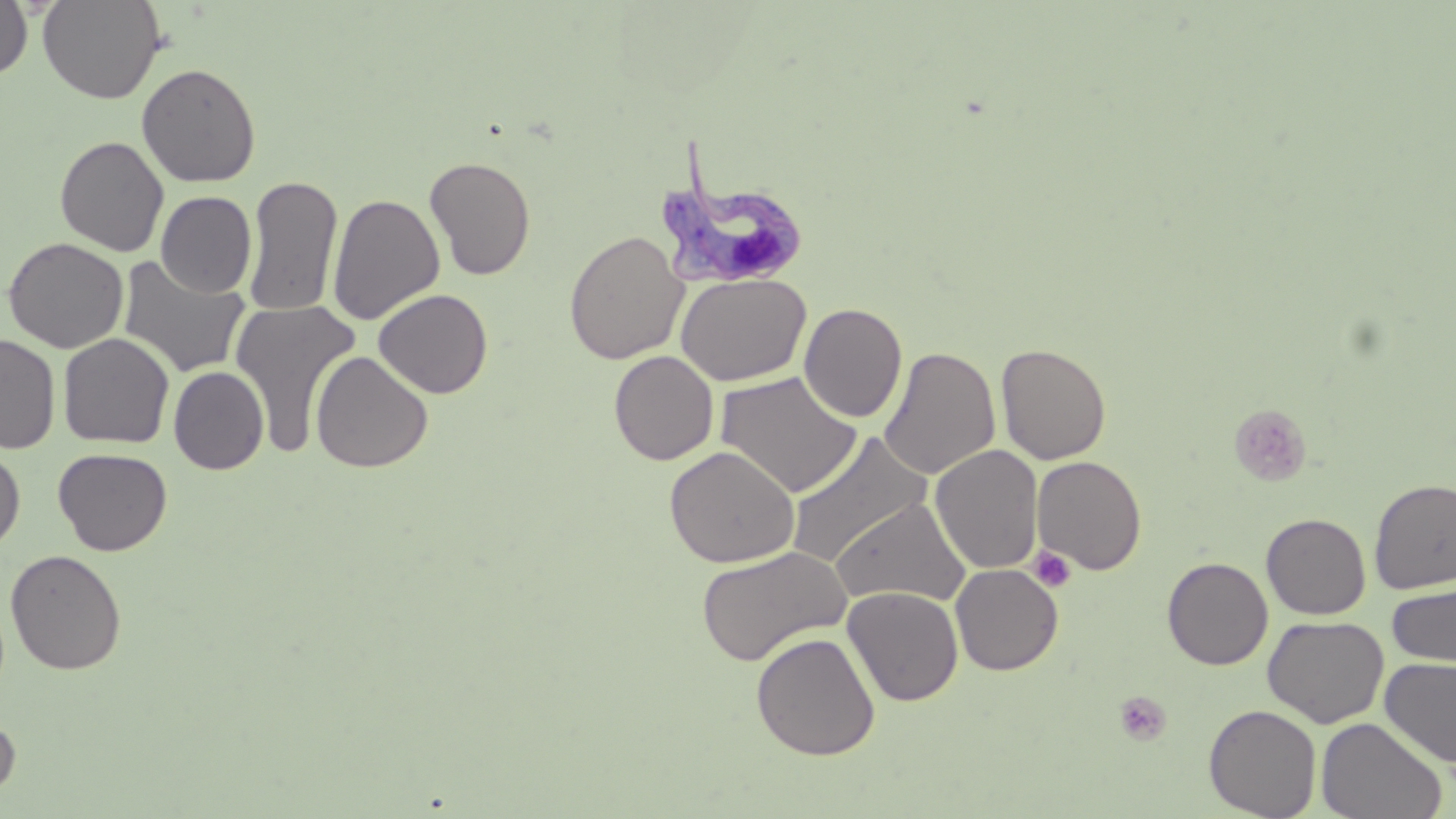

Summary:
  - Coordinate format: approximate bounding boxes as named x1/y1/x2/y2 corners in pixels
  - Platelet locations: (x1=1028, y1=547, x2=1077, y2=593), (x1=1114, y1=691, x2=1172, y2=746)
  - Trypanosoma brucei locations: (x1=654, y1=132, x2=808, y2=290)
  - Uninfected red blood cell locations: (x1=0, y1=0, x2=33, y2=82), (x1=38, y1=0, x2=165, y2=104), (x1=137, y1=62, x2=260, y2=187), (x1=54, y1=135, x2=169, y2=256), (x1=424, y1=156, x2=536, y2=280), (x1=243, y1=175, x2=343, y2=317), (x1=156, y1=191, x2=257, y2=298), (x1=327, y1=192, x2=445, y2=325), (x1=564, y1=230, x2=689, y2=364), (x1=3, y1=237, x2=129, y2=353), (x1=117, y1=255, x2=251, y2=379), (x1=676, y1=273, x2=810, y2=386), (x1=373, y1=288, x2=493, y2=399), (x1=229, y1=299, x2=360, y2=456), (x1=799, y1=303, x2=907, y2=422), (x1=58, y1=333, x2=174, y2=449), (x1=1, y1=335, x2=60, y2=454), (x1=996, y1=342, x2=1111, y2=465), (x1=880, y1=347, x2=1000, y2=479), (x1=310, y1=350, x2=433, y2=473), (x1=609, y1=350, x2=719, y2=465), (x1=168, y1=366, x2=269, y2=475), (x1=715, y1=371, x2=863, y2=498), (x1=786, y1=432, x2=932, y2=568), (x1=663, y1=445, x2=800, y2=568), (x1=930, y1=445, x2=1044, y2=574), (x1=0, y1=447, x2=25, y2=553), (x1=53, y1=448, x2=173, y2=556), (x1=1032, y1=455, x2=1148, y2=575), (x1=1369, y1=478, x2=1456, y2=595), (x1=831, y1=498, x2=971, y2=608), (x1=1261, y1=513, x2=1371, y2=619), (x1=695, y1=544, x2=852, y2=666), (x1=5, y1=549, x2=127, y2=674), (x1=1162, y1=557, x2=1273, y2=670), (x1=950, y1=563, x2=1063, y2=675), (x1=1386, y1=583, x2=1455, y2=669), (x1=843, y1=587, x2=963, y2=706), (x1=1263, y1=615, x2=1388, y2=727), (x1=751, y1=632, x2=880, y2=760), (x1=1380, y1=657, x2=1456, y2=768), (x1=1204, y1=704, x2=1322, y2=818), (x1=0, y1=714, x2=20, y2=801), (x1=1315, y1=717, x2=1448, y2=819)
  - Slide-level diagnosis: Trypanosoma brucei
  - Stain: May-Grünwald-Giemsa
  - Preparation: thin blood smear
  - Field of view: single
  - Image size: 1456×819 pixels
  - Magnification: 1000x
  - Modality: light microscopy